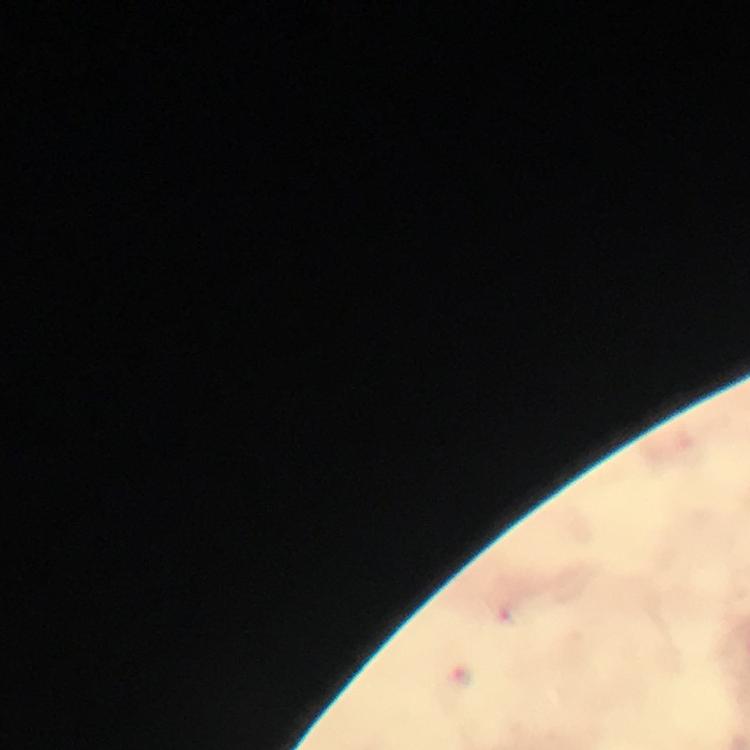

Approximate centers as [x, y] in pixels.
Summary:
  - Plasmodium parasite locations: [460, 677]
  - Stain: Giemsa
  - Cropped from: a single field of view
  - Context: from a malaria diagnostic workup
  - Image size: 750×750 pixels
  - Magnification: 100x
  - Preparation: thick blood film
  - Capture: smartphone camera through the microscope
  - Immersion oil: used